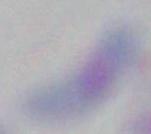
{
  "magnification": "1000x",
  "modality": "photomicrograph",
  "identification": "Toxoplasma gondii"
}